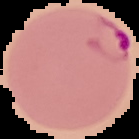
result = Plasmodium parasites detected
preparation = thin blood smear
image type = segmented cell region with the area outside set to black
image size = 139×139 pixels